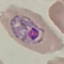
Summary:
  - Result: malaria parasites identified
  - Image type: automatically extracted cell patch, resized to 64 × 64 pixels
  - Capture: smartphone camera at the microscope eyepiece
  - Preparation: thin blood smear
  - Stain: Giemsa